Identify the parasite.
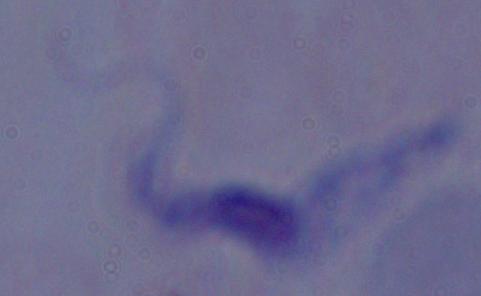
This is a trypanosome.

Summary:
  - Modality: micrograph
  - Magnification: 1000x